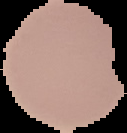

Summary:
  - Image size: 127×133 pixels
  - Preparation: thin blood film
  - Malaria status: uninfected
  - Image type: cell region segmented out of the field of view; surrounding area masked to black